Report the malaria status of this cell.
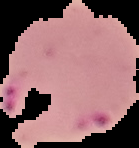
Parasitized.

From a thin blood film. The area outside the segmented cell region is set to black. Image is 139×148 pixels.